Identify the cell.
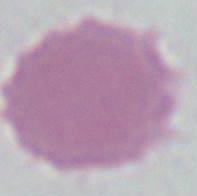
This is an erythrocyte.

Summary:
  - Modality: micrograph
  - Magnification: 1000x